Assess this cell for malaria.
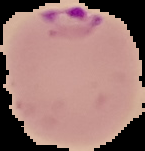
Parasitized.

Cell region segmented out of the field of view; the surrounding area is masked to black. From a thin blood smear. Image is 145×151 pixels.